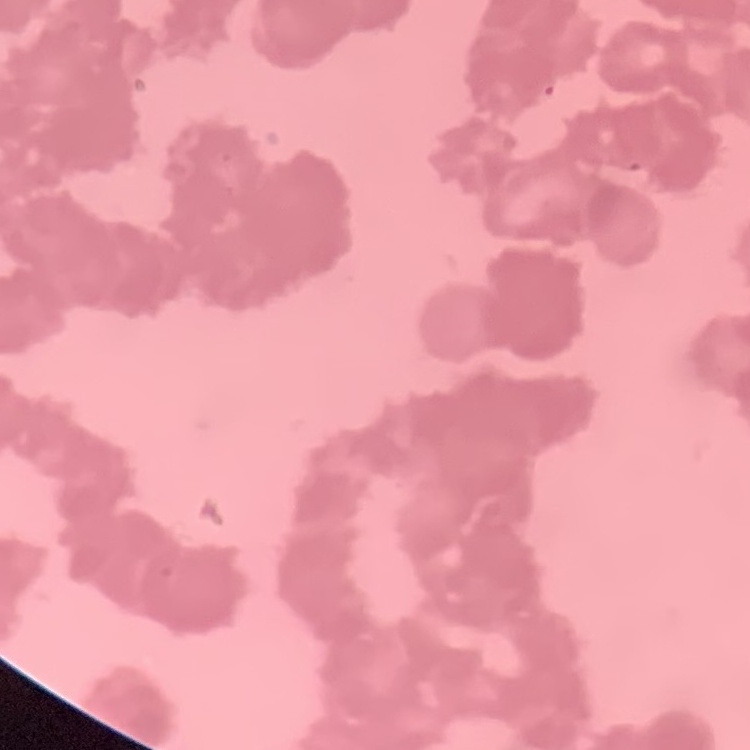

Summary:
  - Erythrocyte morphology: rouleaux formation
  - Image type: one tile cut from a larger photomicrograph
  - Stain: Field's or Giemsa
  - Preparation: thin blood film